Report the malaria status of this cell.
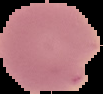
Uninfected.

Summary:
  - Image size: 103×94 pixels
  - Preparation: thin blood smear
  - Image type: segmented cell region with the area outside set to black